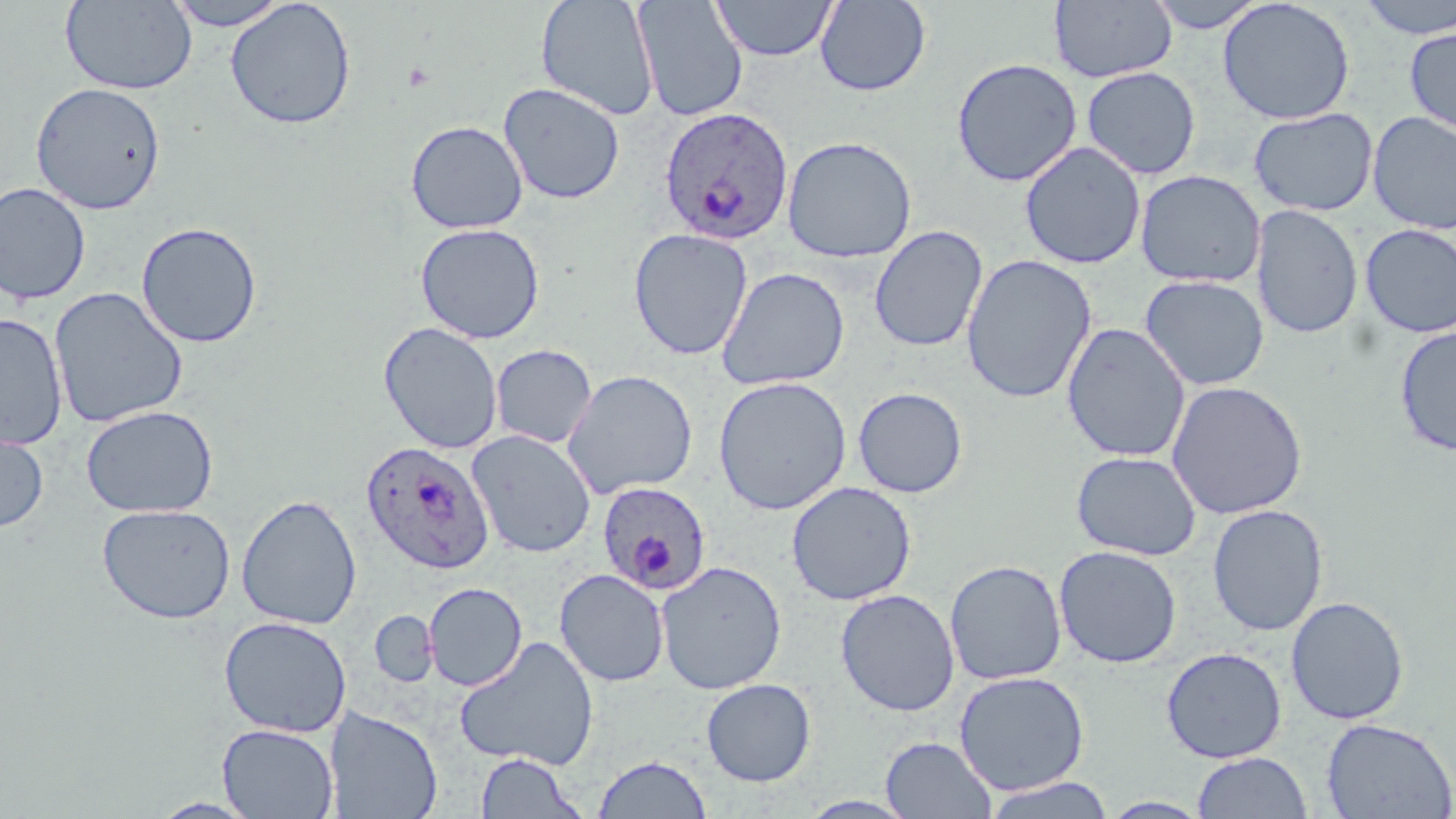

Summary:
  - Coordinate format: approximate bounding boxes as named x1/y1/x2/y2 corners in pixels
  - Uninfected red blood cell locations: (x1=61, y1=0, x2=198, y2=95), (x1=167, y1=0, x2=290, y2=30), (x1=536, y1=0, x2=659, y2=121), (x1=633, y1=0, x2=748, y2=122), (x1=711, y1=0, x2=838, y2=61), (x1=814, y1=0, x2=931, y2=96), (x1=1145, y1=0, x2=1268, y2=33), (x1=1218, y1=0, x2=1356, y2=124), (x1=1352, y1=0, x2=1456, y2=40), (x1=225, y1=1, x2=357, y2=130), (x1=1050, y1=1, x2=1178, y2=83), (x1=1404, y1=25, x2=1456, y2=137), (x1=951, y1=57, x2=1083, y2=187), (x1=1081, y1=66, x2=1201, y2=180), (x1=30, y1=82, x2=166, y2=214), (x1=498, y1=82, x2=625, y2=205), (x1=1248, y1=107, x2=1379, y2=216), (x1=1367, y1=111, x2=1456, y2=235), (x1=406, y1=120, x2=528, y2=234), (x1=781, y1=135, x2=917, y2=263), (x1=1020, y1=141, x2=1146, y2=270), (x1=1135, y1=169, x2=1265, y2=288), (x1=0, y1=182, x2=92, y2=305), (x1=1251, y1=204, x2=1363, y2=340), (x1=135, y1=221, x2=263, y2=348), (x1=415, y1=223, x2=545, y2=344), (x1=1359, y1=224, x2=1456, y2=339), (x1=868, y1=225, x2=988, y2=353), (x1=629, y1=228, x2=753, y2=360), (x1=961, y1=254, x2=1097, y2=404), (x1=716, y1=267, x2=850, y2=390), (x1=1139, y1=274, x2=1269, y2=391), (x1=49, y1=286, x2=188, y2=428), (x1=0, y1=312, x2=68, y2=450), (x1=378, y1=321, x2=503, y2=455), (x1=1062, y1=322, x2=1190, y2=462), (x1=1394, y1=326, x2=1456, y2=455), (x1=490, y1=344, x2=597, y2=448), (x1=562, y1=369, x2=698, y2=500), (x1=713, y1=376, x2=852, y2=515), (x1=1167, y1=380, x2=1307, y2=520), (x1=853, y1=386, x2=968, y2=498), (x1=80, y1=404, x2=218, y2=518), (x1=0, y1=423, x2=49, y2=533), (x1=466, y1=430, x2=596, y2=558), (x1=1071, y1=450, x2=1201, y2=560), (x1=786, y1=480, x2=917, y2=605), (x1=236, y1=493, x2=362, y2=630), (x1=97, y1=503, x2=236, y2=624), (x1=1207, y1=504, x2=1328, y2=636), (x1=1053, y1=545, x2=1182, y2=668), (x1=944, y1=559, x2=1067, y2=686), (x1=656, y1=560, x2=787, y2=694), (x1=554, y1=569, x2=670, y2=687), (x1=424, y1=582, x2=527, y2=691), (x1=835, y1=588, x2=960, y2=716), (x1=1285, y1=596, x2=1409, y2=725), (x1=370, y1=610, x2=439, y2=687), (x1=219, y1=616, x2=351, y2=737), (x1=453, y1=635, x2=600, y2=771), (x1=1161, y1=646, x2=1287, y2=763), (x1=953, y1=670, x2=1090, y2=795), (x1=701, y1=678, x2=817, y2=786), (x1=325, y1=706, x2=443, y2=819), (x1=1321, y1=716, x2=1456, y2=819), (x1=217, y1=724, x2=339, y2=818), (x1=881, y1=737, x2=997, y2=818), (x1=1192, y1=751, x2=1312, y2=818), (x1=475, y1=752, x2=587, y2=819), (x1=592, y1=754, x2=712, y2=818), (x1=981, y1=777, x2=1116, y2=819), (x1=1099, y1=797, x2=1213, y2=818), (x1=149, y1=798, x2=261, y2=818)
  - Plasmodium ovale-infected red blood cell locations: (x1=659, y1=106, x2=794, y2=245), (x1=361, y1=440, x2=495, y2=574), (x1=596, y1=481, x2=712, y2=595)
  - Slide-level diagnosis: Plasmodium ovale
  - Stain: May-Grünwald-Giemsa
  - Field of view: single
  - Modality: optical microscopy
  - Preparation: thin blood smear
  - Magnification: 1000x
  - Image size: 1456×819 pixels